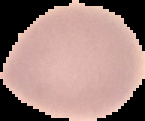

{
  "image_size": "145×121 pixels",
  "preparation": "thin blood film",
  "image_type": "segmented cell region on a black background",
  "result": "negative for Plasmodium parasites"
}